Assess this cell for malaria.
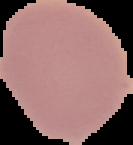

Uninfected.

preparation = thin blood smear
image type = cell region segmented out of the field of view; surrounding area masked to black
image size = 133×145 pixels